Locate every leukocyte (white blood cell).
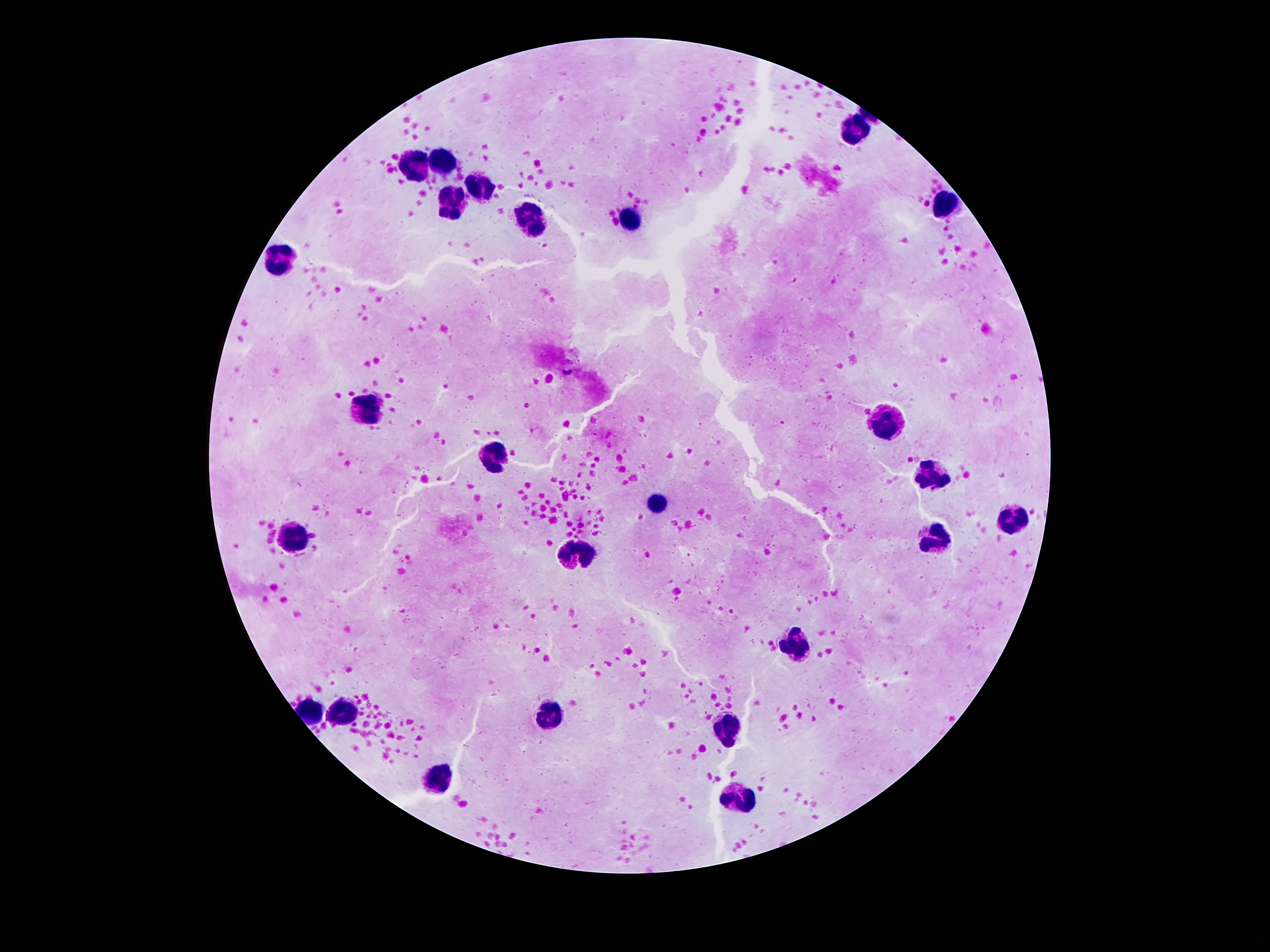

Approximate object centers, in pixels from the top-left corner.
Leukocytes: (x=856, y=132), (x=446, y=164), (x=416, y=166), (x=477, y=187), (x=452, y=201), (x=942, y=203), (x=629, y=217), (x=532, y=225), (x=280, y=258), (x=368, y=412), (x=890, y=423), (x=493, y=454), (x=924, y=476), (x=656, y=505), (x=1011, y=522), (x=298, y=538), (x=936, y=539), (x=579, y=550), (x=797, y=645), (x=348, y=711), (x=550, y=713), (x=727, y=731), (x=443, y=780), (x=738, y=801).

100x magnification. Image is 1270×952 pixels. Patient malaria status: not infected. Giemsa stain. Single field of view. Smartphone photograph taken through the microscope eyepiece. Thick blood film.